Outline platelets.
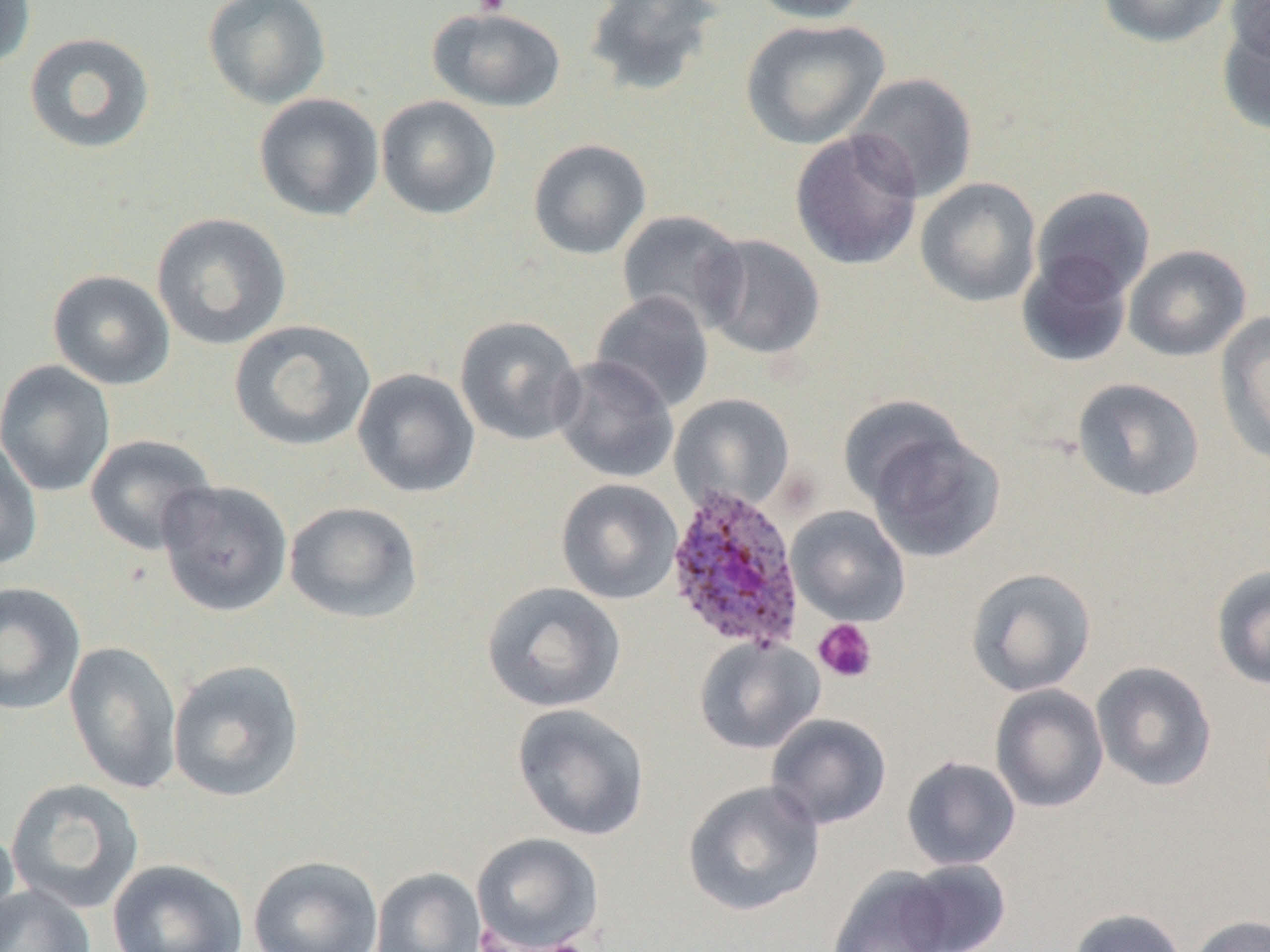
Approximate bounding boxes as (x1, y1, x2, y2) in pixels.
Platelets: (470, 0, 514, 17), (813, 618, 877, 683).

Summary:
  - Plasmodium ovale-infected red blood cell locations: (664, 484, 806, 654)
  - Uninfected red blood cell locations: (0, 0, 36, 73), (202, 0, 331, 109), (583, 0, 724, 98), (748, 0, 873, 24), (1097, 0, 1233, 48), (1226, 1, 1270, 65), (427, 6, 567, 112), (1217, 17, 1270, 138), (740, 18, 889, 150), (24, 31, 156, 155), (847, 72, 979, 203), (253, 93, 384, 221), (376, 95, 501, 220), (790, 129, 923, 271), (528, 138, 652, 260), (916, 177, 1042, 308), (1031, 185, 1155, 303), (616, 209, 749, 333), (151, 212, 292, 350), (699, 233, 825, 360), (1123, 244, 1251, 362), (1017, 251, 1133, 367), (48, 269, 175, 390), (590, 291, 715, 413), (1216, 311, 1270, 465), (454, 315, 585, 446), (229, 319, 376, 451), (551, 356, 679, 483), (0, 360, 116, 497), (351, 368, 480, 498), (1072, 378, 1205, 502), (669, 394, 795, 515), (837, 394, 969, 509), (864, 427, 1005, 563), (84, 434, 219, 555), (0, 437, 43, 572), (555, 478, 682, 605), (157, 480, 293, 617), (284, 501, 424, 624), (787, 506, 910, 626), (1210, 565, 1270, 691), (966, 567, 1097, 697), (0, 581, 86, 716), (481, 581, 625, 713), (694, 636, 824, 754), (64, 641, 183, 794), (168, 659, 305, 802), (1091, 661, 1218, 792), (990, 684, 1109, 813), (511, 703, 650, 841), (765, 713, 892, 829), (901, 755, 1021, 871), (5, 778, 145, 914), (682, 779, 825, 916), (0, 823, 21, 944), (471, 833, 604, 952), (248, 855, 384, 952), (106, 858, 248, 952), (897, 859, 1012, 951), (827, 866, 958, 952), (370, 867, 486, 952), (0, 884, 95, 952), (1068, 907, 1186, 952), (1188, 914, 1270, 952)
  - Slide-level diagnosis: Plasmodium ovale
  - Preparation: thin blood smear
  - Modality: light microscopy
  - Field of view: single
  - Image size: 1270×952 pixels
  - Magnification: 1000x